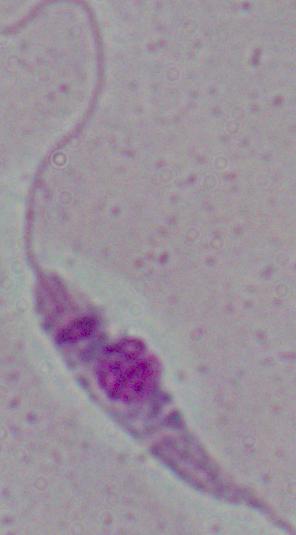
identification = Leishmania
modality = photomicrograph
magnification = 1000x